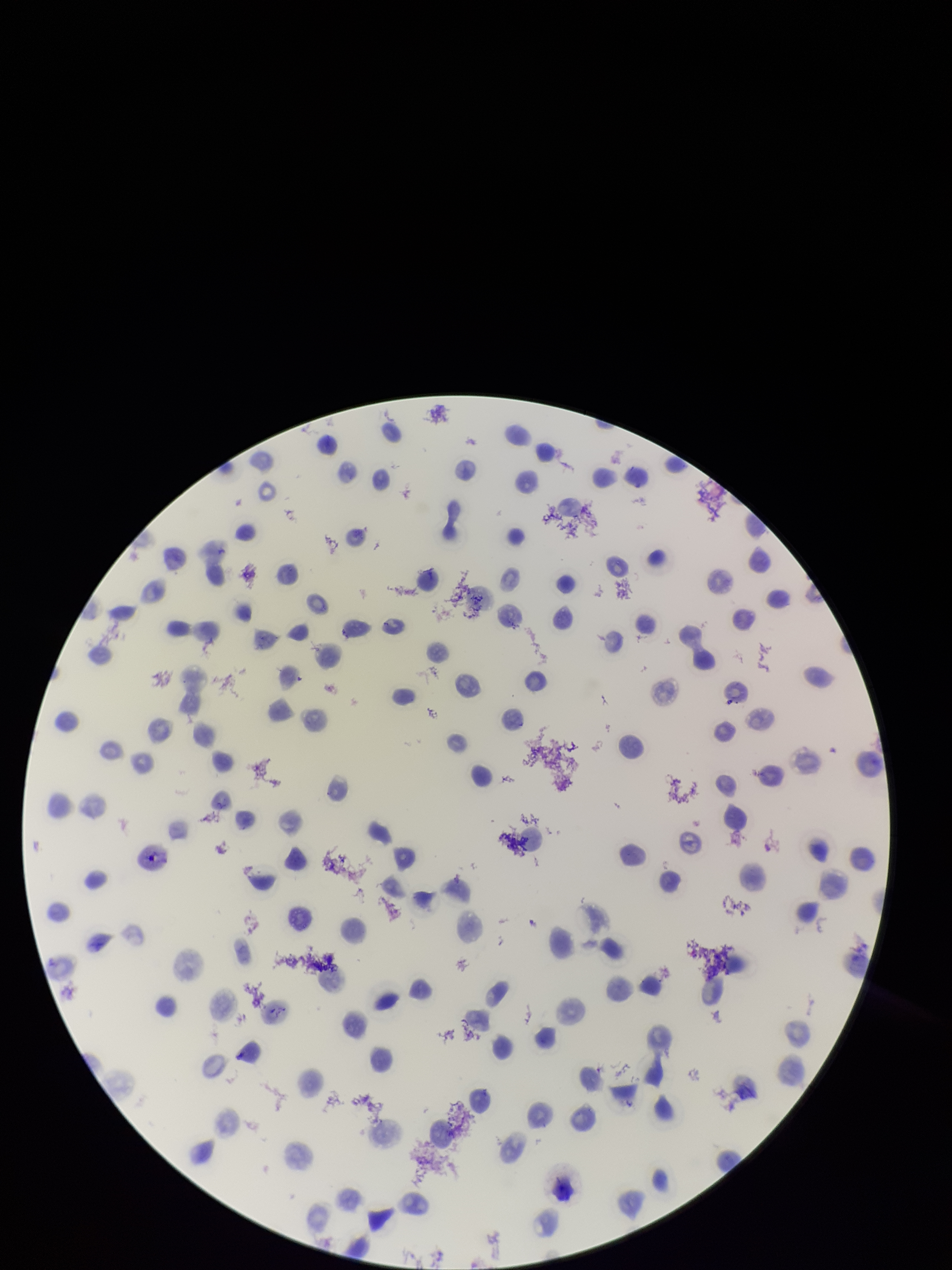
Species reported for this patient: Plasmodium vivax. Patient malaria status: infected. Red blood cell count: 94. Photographed through the microscope eyepiece with a smartphone camera. Parasitized red blood cells: none identified. Image is 952×1270 pixels. One field from this slide. Parasitized red blood cell count: 0. Giemsa stain. Preparation: thin smear.